Comment on the morphology of the erythrocytes.
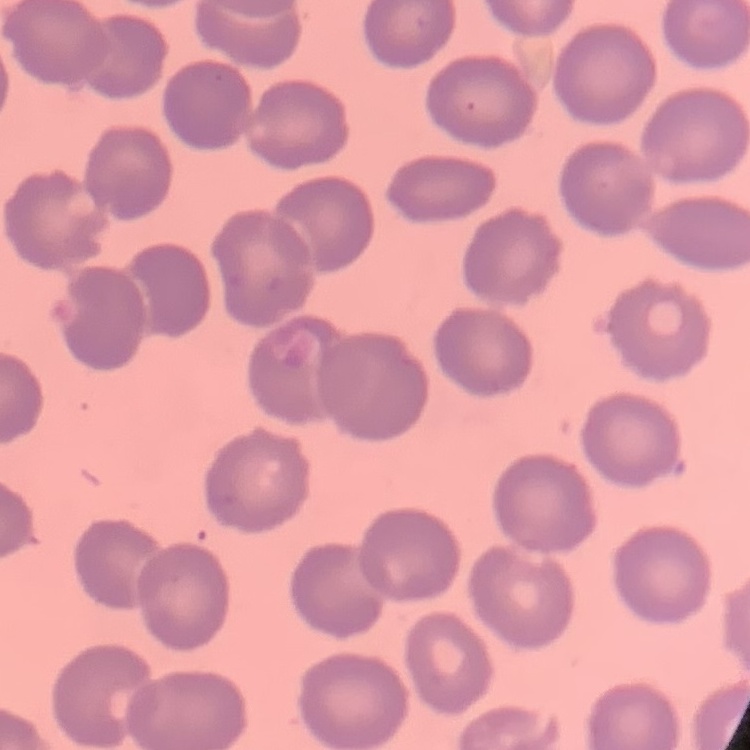

No rouleaux formation.

Summary:
  - Image type: one tile cut from a larger photomicrograph
  - Stain: Field's or Giemsa
  - Preparation: thin blood film